Name the parasite shown.
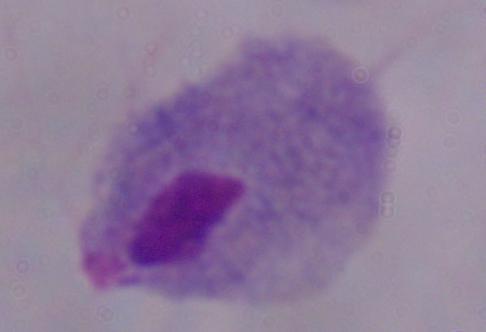
This is a trichomonad.

Captured at 1000x magnification. Photomicrograph.